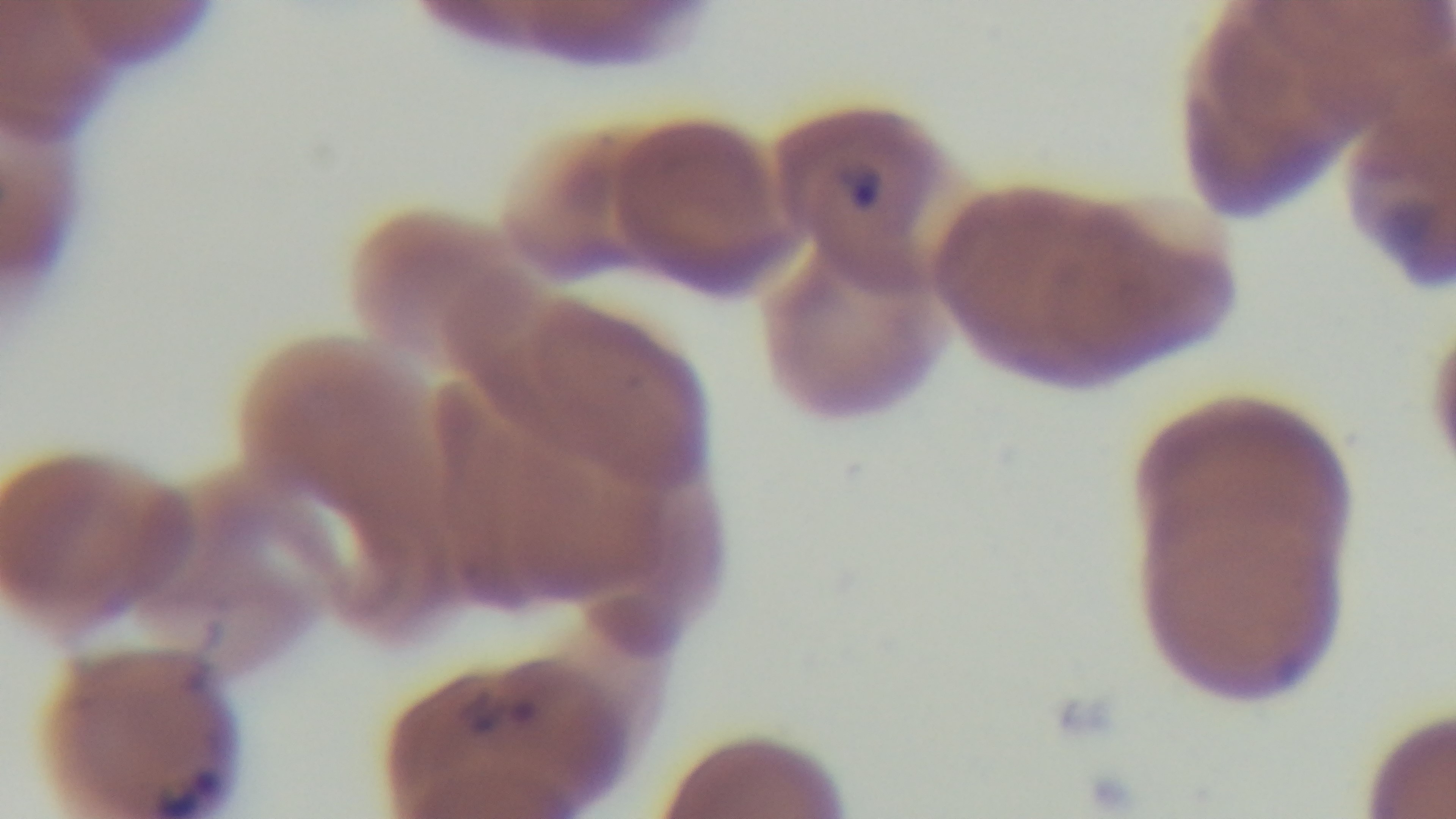
{
  "stain": "Giemsa",
  "preparation": "thin blood film",
  "modality": "light microscopy",
  "field_of_view": "one from the slide",
  "capture": "mounted 4K digital camera",
  "objective": "100x oil immersion",
  "malaria_status": "infected"
}